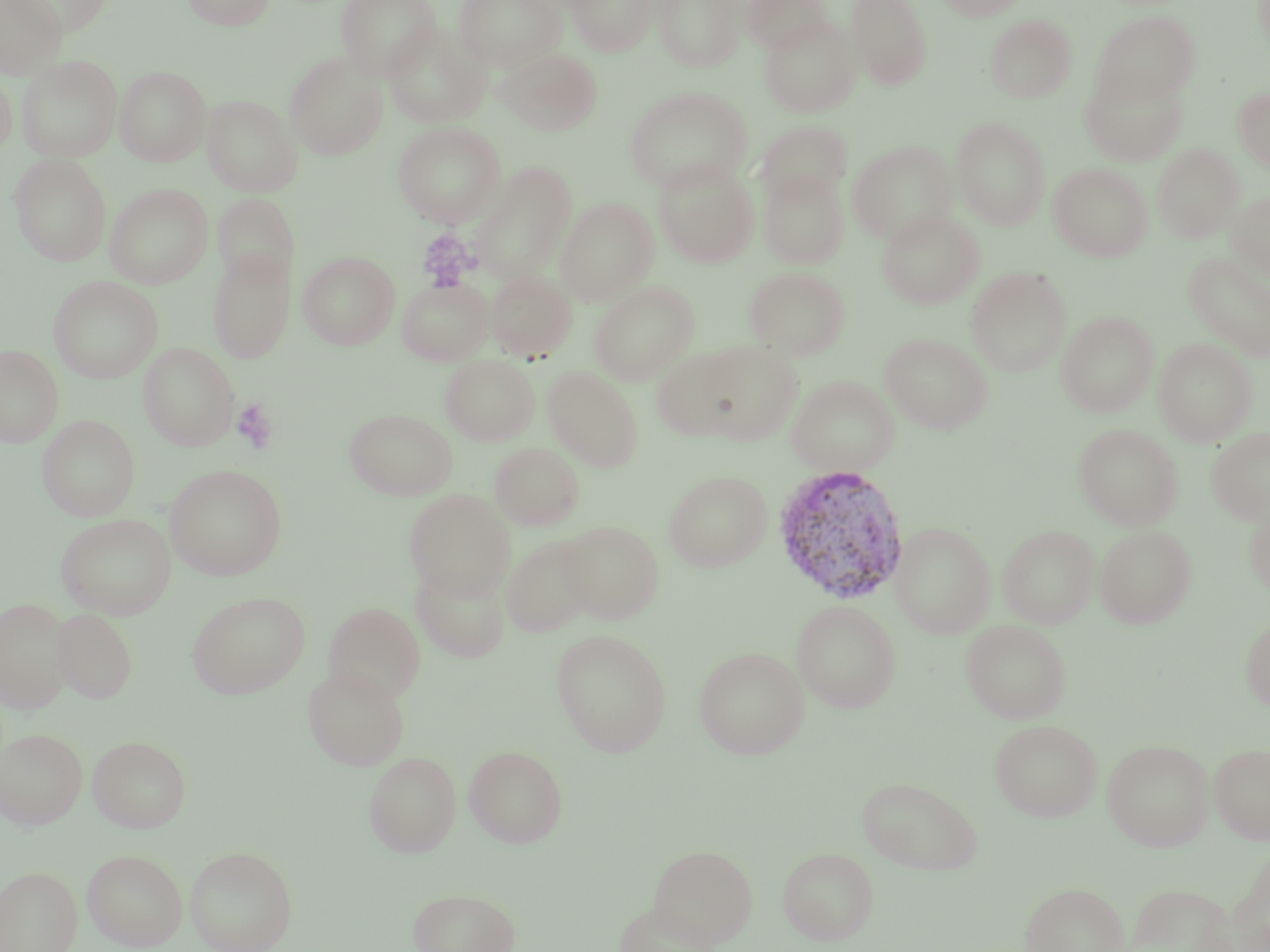
Summary:
  - Coordinate format: approximate bounding boxes as [x1, y1, x2, y2] in pixels
  - Plasmodium vivax-infected red blood cell locations: [771, 463, 911, 606]
  - Platelet locations: [417, 228, 476, 290], [230, 398, 278, 454]
  - Uninfected red blood cell locations: [0, 0, 67, 78], [10, 0, 114, 36], [181, 0, 276, 30], [335, 0, 441, 81], [454, 0, 565, 72], [566, 0, 659, 55], [652, 0, 746, 71], [742, 0, 831, 54], [846, 0, 932, 89], [937, 0, 1026, 21], [1091, 10, 1198, 105], [759, 15, 860, 117], [986, 15, 1076, 102], [382, 22, 491, 128], [496, 48, 601, 135], [284, 52, 388, 159], [17, 55, 122, 162], [115, 66, 210, 166], [0, 67, 16, 159], [1080, 68, 1188, 167], [624, 86, 751, 193], [1233, 86, 1270, 172], [202, 95, 302, 196], [951, 117, 1050, 229], [757, 121, 852, 206], [393, 122, 505, 227], [848, 141, 958, 245], [1152, 144, 1244, 242], [9, 153, 112, 266], [470, 160, 577, 284], [653, 160, 759, 268], [1049, 163, 1152, 261], [758, 169, 849, 269], [105, 184, 213, 288], [1227, 190, 1270, 280], [212, 193, 299, 287], [555, 197, 658, 304], [878, 210, 984, 309], [208, 246, 295, 363], [298, 251, 399, 349], [1185, 252, 1270, 361], [745, 266, 849, 359], [967, 266, 1071, 377], [487, 268, 576, 361], [49, 276, 163, 383], [397, 278, 492, 365], [589, 281, 699, 385], [1057, 311, 1158, 417], [880, 333, 991, 433], [1153, 338, 1256, 446], [694, 341, 803, 445], [139, 343, 239, 450], [0, 344, 63, 447], [651, 348, 743, 439], [440, 356, 539, 445], [543, 366, 643, 471], [786, 376, 899, 477], [345, 408, 457, 500], [38, 415, 139, 521], [1073, 424, 1182, 530], [1206, 428, 1270, 525], [490, 442, 584, 529], [165, 464, 287, 580], [664, 470, 772, 572], [404, 490, 514, 599], [1244, 498, 1270, 599], [55, 513, 176, 619], [559, 520, 664, 623], [890, 522, 995, 638], [998, 525, 1099, 628], [1095, 525, 1196, 628], [502, 534, 597, 637], [410, 562, 511, 663], [187, 591, 310, 698], [0, 596, 72, 714], [791, 600, 901, 713], [323, 602, 426, 704], [53, 608, 137, 704], [1241, 615, 1270, 712], [961, 620, 1071, 723], [551, 629, 672, 756], [694, 645, 809, 759], [303, 664, 410, 770], [989, 719, 1103, 821], [0, 727, 88, 829], [88, 735, 191, 832], [1102, 739, 1214, 851], [1208, 742, 1270, 843], [464, 745, 568, 847], [364, 751, 461, 858], [857, 776, 982, 874], [648, 843, 757, 947], [185, 845, 298, 952], [1223, 845, 1270, 952], [777, 846, 879, 945], [82, 849, 187, 950], [0, 866, 82, 952], [1020, 882, 1128, 952], [1123, 883, 1239, 952], [408, 887, 521, 952], [614, 901, 719, 952]
  - Slide-level diagnosis: Plasmodium vivax
  - Image size: 1270×952 pixels
  - Stain: May-Grünwald-Giemsa
  - Magnification: 1000x
  - Preparation: thin blood film
  - Field of view: one of a larger specimen
  - Modality: light microscopy